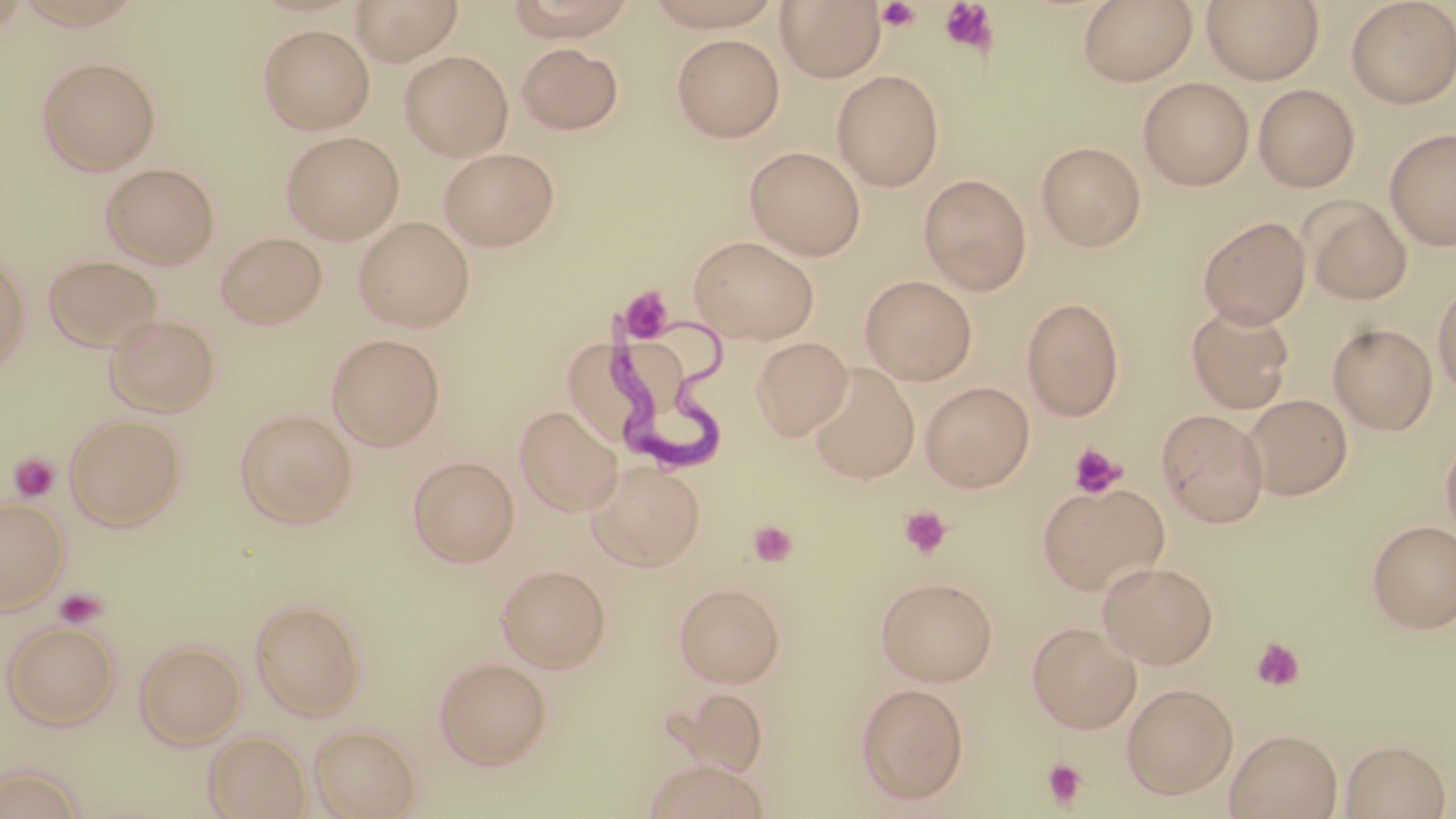 Approximate bounding boxes as (x1, y1, x2, y2) in pixels. Uninfected red blood cell locations: (350, 0, 464, 64), (500, 0, 643, 40), (636, 0, 788, 31), (1077, 0, 1198, 85), (1201, 0, 1324, 84), (775, 1, 886, 82), (1345, 1, 1456, 108), (258, 24, 374, 134), (671, 34, 785, 142), (515, 42, 624, 134), (399, 50, 514, 160), (37, 57, 161, 175), (832, 69, 944, 190), (1138, 77, 1254, 190), (1253, 84, 1360, 192), (1384, 127, 1456, 250), (281, 130, 404, 243), (1035, 140, 1146, 251), (745, 145, 866, 259), (437, 147, 560, 251), (100, 162, 220, 268), (919, 173, 1032, 294), (1302, 198, 1412, 305), (353, 216, 475, 332), (1198, 216, 1311, 327), (215, 231, 327, 331), (688, 235, 820, 343), (43, 254, 163, 351), (0, 255, 30, 373), (860, 274, 978, 385), (1432, 279, 1456, 396), (1022, 296, 1125, 421), (1186, 302, 1295, 413), (103, 313, 221, 417), (1328, 324, 1437, 434), (326, 333, 446, 451), (751, 336, 853, 440), (806, 363, 921, 483), (920, 380, 1035, 491), (1242, 394, 1353, 500), (515, 405, 622, 515), (235, 408, 358, 528), (1156, 409, 1269, 526), (63, 414, 187, 530), (1440, 433, 1456, 540), (408, 454, 519, 567), (586, 460, 705, 570), (1037, 481, 1169, 596), (0, 496, 68, 611), (1368, 519, 1456, 632), (1097, 560, 1219, 668), (496, 563, 611, 672), (875, 575, 998, 686), (674, 582, 786, 687), (249, 598, 365, 720), (2, 619, 120, 730), (1027, 621, 1141, 733), (134, 639, 245, 748), (434, 657, 551, 769), (856, 682, 970, 805), (1122, 683, 1238, 798), (668, 685, 769, 777), (308, 723, 421, 818), (1225, 728, 1342, 818), (204, 729, 311, 819), (1340, 739, 1451, 818), (642, 758, 769, 819), (0, 764, 88, 818). Platelet locations: (938, 0, 998, 56), (874, 1, 924, 32), (619, 286, 675, 342), (1067, 442, 1127, 499), (9, 452, 61, 502), (899, 506, 952, 558), (749, 520, 797, 566), (53, 587, 109, 629), (1251, 637, 1305, 691), (1041, 758, 1089, 809). Trypanosoma brucei locations: (602, 310, 729, 487). Slide-level diagnosis: Trypanosoma brucei. One field of a larger specimen. 1000x magnification. May-Grünwald-Giemsa stain. Light microscopy. Thin blood smear. Image is 1456×819 pixels.